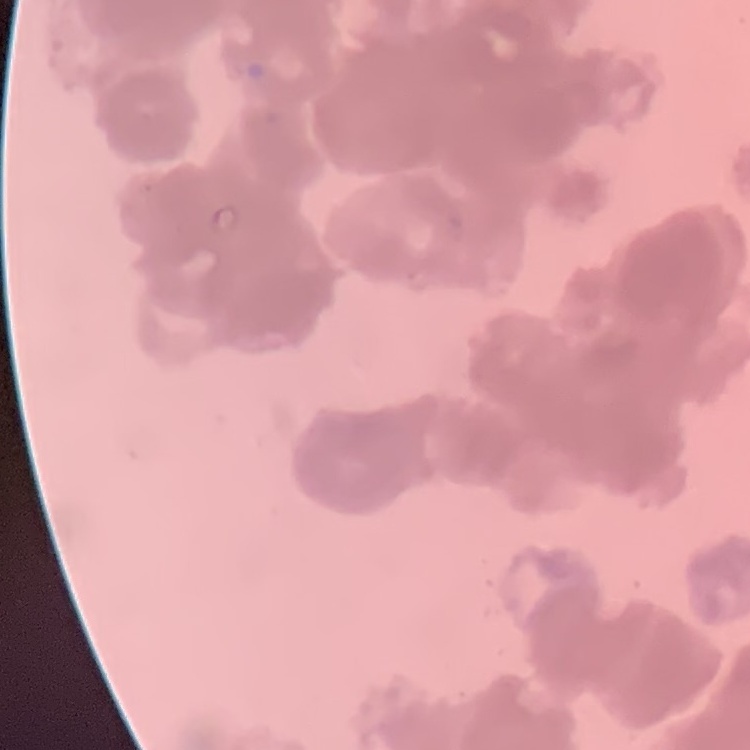

red blood cell morphology = rouleaux formation
image type = square crop of a larger photomicrograph
stain = Field's or Giemsa
preparation = thin blood smear